Identify the cell.
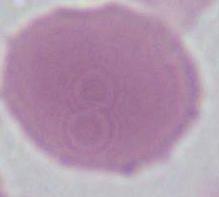
This is an erythrocyte.

Summary:
  - Magnification: 1000x
  - Modality: photomicrograph